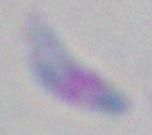

modality = photomicrograph
magnification = 1000x
identification = Toxoplasma gondii